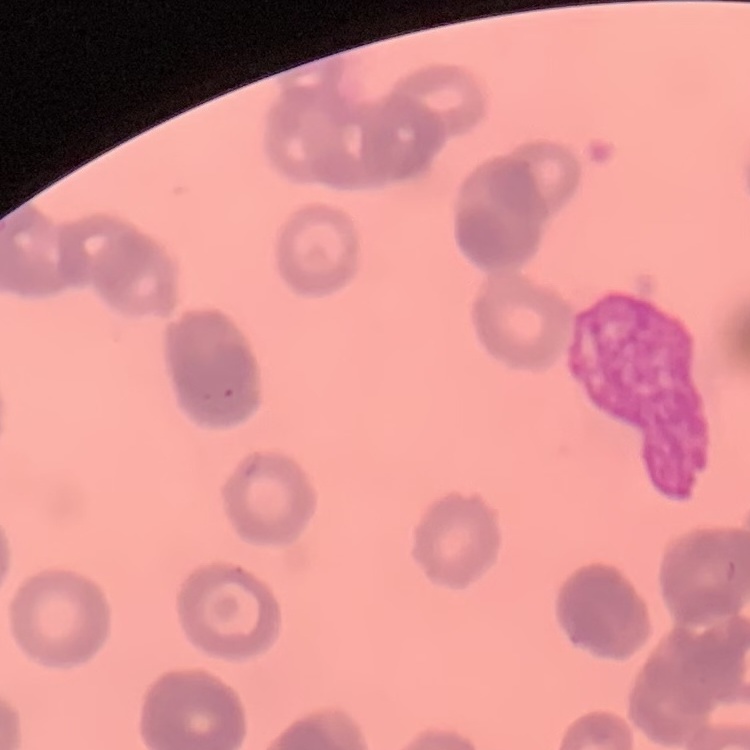

The red blood cells exhibit rouleaux formation. Field's or Giemsa stain. Square crop of a larger photomicrograph. Thin blood smear.